State the blood parasite species.
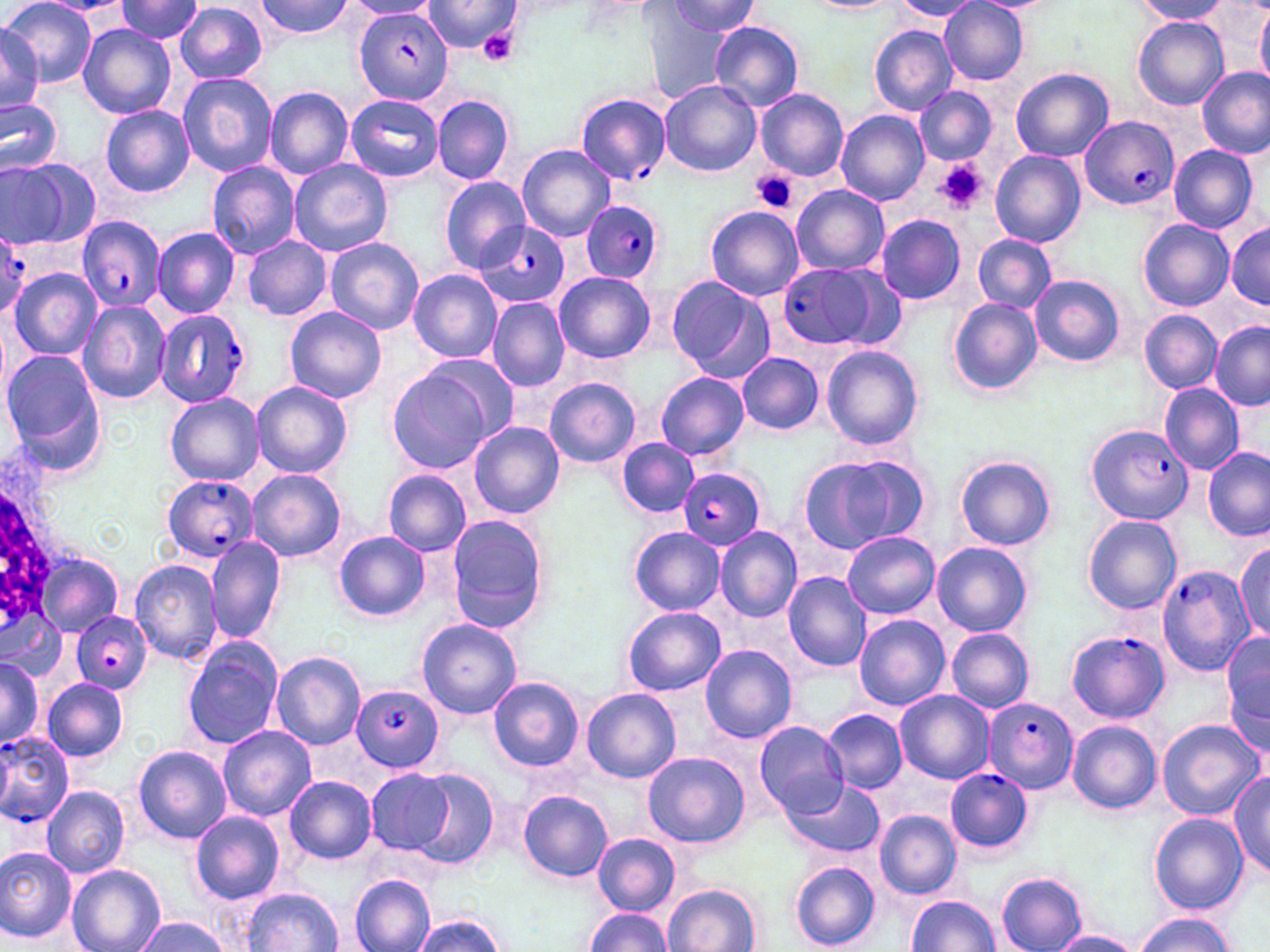
Plasmodium falciparum.

uninfected red blood cell locations = approximate bounding boxes as [x1, y1, x2, y2] in pixels: [1, 0, 97, 87], [249, 0, 358, 41], [420, 0, 520, 57], [1133, 0, 1232, 25], [116, 1, 205, 44], [889, 1, 983, 22], [939, 1, 1029, 85], [344, 2, 440, 20], [660, 2, 763, 39], [802, 2, 900, 13], [176, 4, 268, 82], [645, 6, 737, 104], [1257, 6, 1270, 88], [1133, 16, 1227, 110], [709, 21, 804, 112], [0, 23, 48, 115], [78, 24, 176, 119], [870, 26, 957, 115], [1011, 67, 1113, 162], [1196, 67, 1269, 159], [177, 73, 278, 177], [659, 80, 761, 177], [914, 86, 998, 167], [264, 87, 354, 180], [755, 90, 848, 181], [345, 94, 442, 182], [433, 94, 514, 185], [0, 98, 62, 175], [101, 105, 195, 197], [835, 110, 929, 205], [1167, 142, 1258, 233], [516, 144, 614, 242], [992, 151, 1086, 246], [1, 158, 98, 248], [288, 159, 394, 259], [206, 161, 300, 259], [439, 176, 529, 272], [791, 184, 889, 276], [705, 206, 804, 301], [875, 214, 968, 305], [1138, 219, 1234, 311], [1227, 220, 1270, 312], [152, 226, 241, 318], [973, 234, 1055, 313], [243, 236, 332, 321], [323, 236, 424, 336], [8, 268, 100, 361], [407, 270, 502, 362], [553, 271, 655, 363], [1029, 275, 1126, 367], [666, 276, 773, 384], [487, 298, 570, 392], [947, 298, 1042, 395], [78, 300, 170, 404], [283, 306, 387, 405], [1146, 309, 1230, 471], [1140, 310, 1221, 394], [1210, 323, 1270, 410], [821, 345, 924, 451], [0, 349, 104, 466], [419, 352, 518, 446], [737, 353, 823, 435], [387, 368, 494, 474], [654, 371, 750, 461], [545, 377, 641, 468], [250, 382, 352, 478], [1158, 384, 1245, 475], [165, 394, 264, 484], [468, 420, 564, 518], [615, 439, 699, 518], [1203, 448, 1269, 541], [798, 451, 931, 554], [955, 455, 1057, 550], [247, 469, 346, 562], [382, 469, 472, 556], [348, 484, 457, 603], [1083, 516, 1181, 614], [446, 517, 549, 633], [714, 526, 803, 622], [627, 527, 725, 614], [333, 531, 430, 623], [841, 532, 940, 619], [204, 536, 285, 644], [1233, 540, 1269, 644], [931, 541, 1033, 637], [34, 550, 123, 637], [128, 558, 223, 664], [782, 571, 874, 673], [621, 607, 727, 697], [2, 615, 68, 683], [853, 615, 950, 710], [417, 618, 521, 720], [945, 628, 1035, 714], [1222, 631, 1270, 748], [182, 637, 285, 749], [700, 645, 798, 742], [269, 650, 368, 751], [0, 656, 44, 751], [488, 676, 583, 771], [42, 678, 129, 762], [581, 688, 681, 783], [895, 690, 994, 783], [823, 708, 907, 792], [1156, 719, 1263, 821], [755, 720, 849, 819], [1066, 721, 1161, 813], [217, 725, 316, 819], [133, 745, 231, 844], [643, 752, 749, 849], [365, 768, 453, 856], [408, 768, 500, 870], [1229, 771, 1270, 881], [284, 776, 377, 863], [782, 777, 886, 859], [42, 786, 130, 878], [518, 789, 613, 881], [875, 810, 962, 898], [189, 811, 286, 904], [1150, 813, 1248, 914], [593, 833, 681, 916], [0, 848, 76, 942], [790, 862, 881, 950], [67, 865, 165, 952], [997, 873, 1088, 952], [350, 875, 436, 952], [663, 883, 761, 952], [242, 889, 343, 951], [905, 895, 1000, 951], [584, 908, 674, 950], [1135, 913, 1235, 952], [413, 916, 506, 952], [134, 917, 231, 952], [1048, 931, 1142, 952]
image size = 1270×952 pixels
white blood cell locations = approximate bounding boxes as [x1, y1, x2, y2] in pixels: [0, 441, 71, 646]
modality = optical microscopy
stain = May-Grünwald-Giemsa
platelet locations = approximate bounding boxes as [x1, y1, x2, y2] in pixels: [477, 26, 521, 66], [935, 158, 989, 213], [752, 169, 800, 214]
magnification = 1000x
preparation = thin blood film
field of view = one of a larger specimen
Plasmodium falciparum-infected red blood cell locations = approximate bounding boxes as [x1, y1, x2, y2] in pixels: [357, 4, 453, 107], [577, 92, 671, 186], [1080, 116, 1179, 210], [582, 199, 665, 285], [77, 216, 167, 313], [477, 220, 569, 309], [0, 224, 31, 321], [778, 263, 888, 351], [154, 308, 251, 409], [1084, 423, 1192, 523], [677, 468, 766, 549], [161, 474, 260, 562], [1156, 565, 1254, 677], [72, 610, 151, 693], [1066, 630, 1169, 721], [351, 685, 445, 772], [983, 696, 1077, 794], [0, 729, 75, 827], [944, 767, 1032, 854]